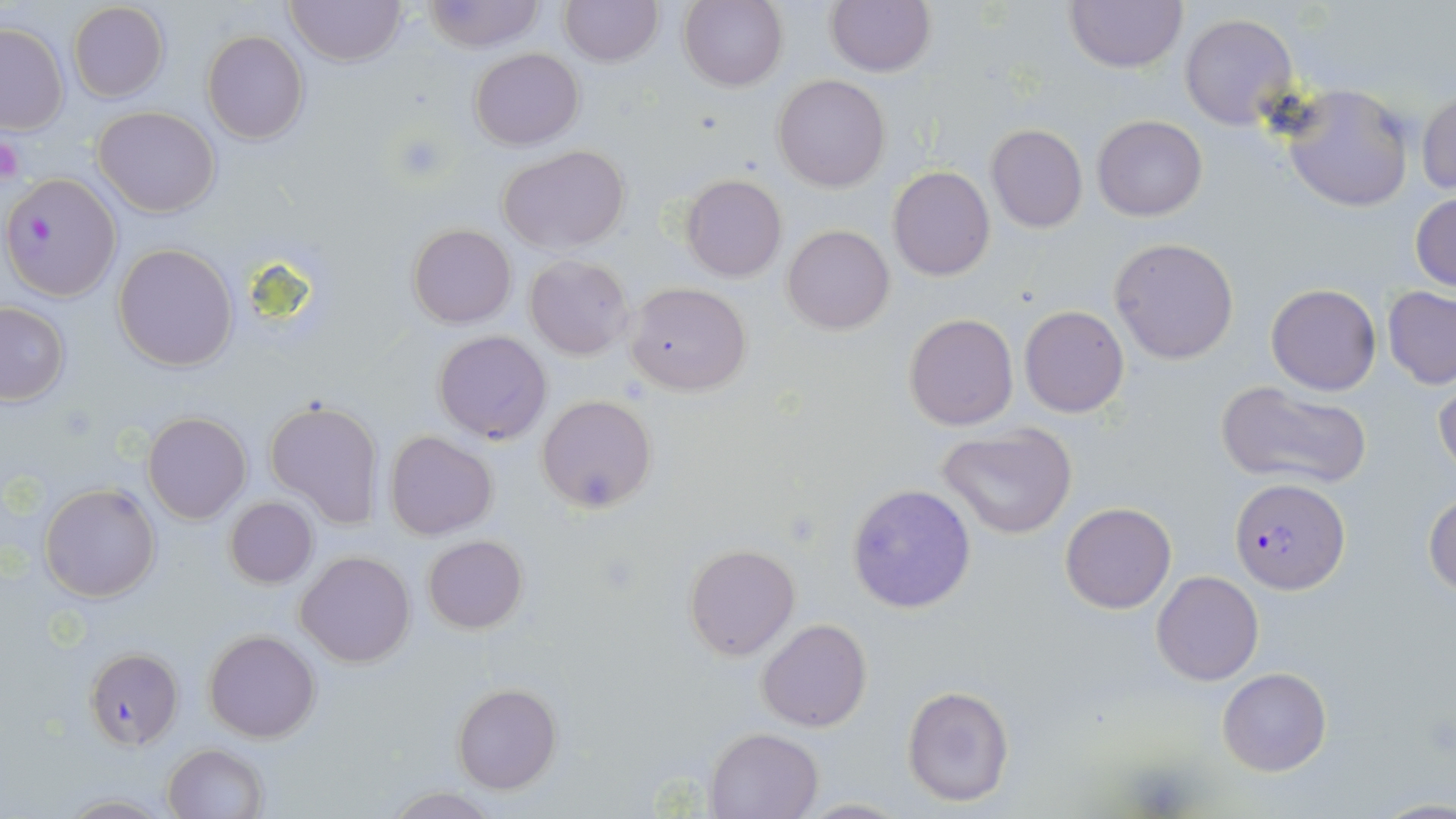

Approximate bounding boxes as [x1, y1, x2, y2] in pixels. Platelet locations: [0, 132, 24, 185], [1128, 763, 1194, 815]. Uninfected red blood cell locations: [285, 0, 405, 67], [421, 0, 546, 52], [558, 0, 662, 67], [680, 0, 788, 91], [825, 0, 935, 77], [1064, 0, 1186, 72], [68, 2, 170, 102], [1180, 13, 1298, 131], [0, 23, 69, 133], [200, 30, 309, 144], [470, 47, 584, 150], [773, 74, 891, 192], [1281, 84, 1416, 213], [1416, 90, 1456, 194], [94, 105, 219, 216], [1092, 115, 1207, 221], [985, 124, 1087, 233], [499, 143, 629, 254], [888, 166, 994, 281], [680, 174, 787, 282], [1411, 190, 1456, 294], [406, 223, 516, 328], [783, 225, 895, 334], [1109, 237, 1240, 365], [113, 244, 239, 370], [525, 255, 633, 361], [624, 282, 752, 395], [1265, 284, 1381, 395], [1382, 287, 1456, 388], [0, 303, 69, 405], [1018, 305, 1131, 418], [903, 313, 1018, 430], [433, 330, 552, 445], [1433, 379, 1455, 481], [1215, 380, 1372, 490], [537, 394, 657, 512], [264, 398, 384, 529], [144, 412, 251, 523], [938, 424, 1077, 538], [384, 430, 498, 540], [846, 482, 976, 615], [41, 483, 162, 602], [1424, 494, 1456, 596], [224, 497, 318, 587], [1062, 502, 1176, 614], [423, 535, 528, 634], [683, 543, 800, 661], [296, 551, 416, 667], [1151, 571, 1263, 686], [756, 618, 872, 733], [204, 629, 320, 743], [83, 648, 182, 749], [1216, 667, 1331, 776], [453, 682, 562, 794], [901, 684, 1015, 808], [703, 728, 822, 817], [162, 744, 270, 819], [380, 787, 502, 817], [56, 793, 174, 817], [792, 796, 910, 817]. Plasmodium falciparum-infected red blood cell locations: [2, 172, 123, 302], [1229, 478, 1350, 593]. Slide-level diagnosis: Plasmodium falciparum. Light microscopy. May-Grünwald-Giemsa-stained preparation. Image is 1456×819 pixels. One field of a larger specimen. Captured at 1000x magnification. Thin blood smear.